Assess this cell for malaria.
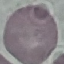
Uninfected.

{
  "image_type": "automatically extracted cell patch, resized to 64 × 64 pixels",
  "capture": "smartphone through the microscope eyepiece",
  "preparation": "thin blood film",
  "stain": "Giemsa"
}